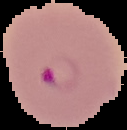

Summary:
  - Image size: 127×130 pixels
  - Image type: segmented cell region on a black background
  - Result: malaria parasites identified
  - Preparation: thin blood film